Locate every Plasmodium parasite.
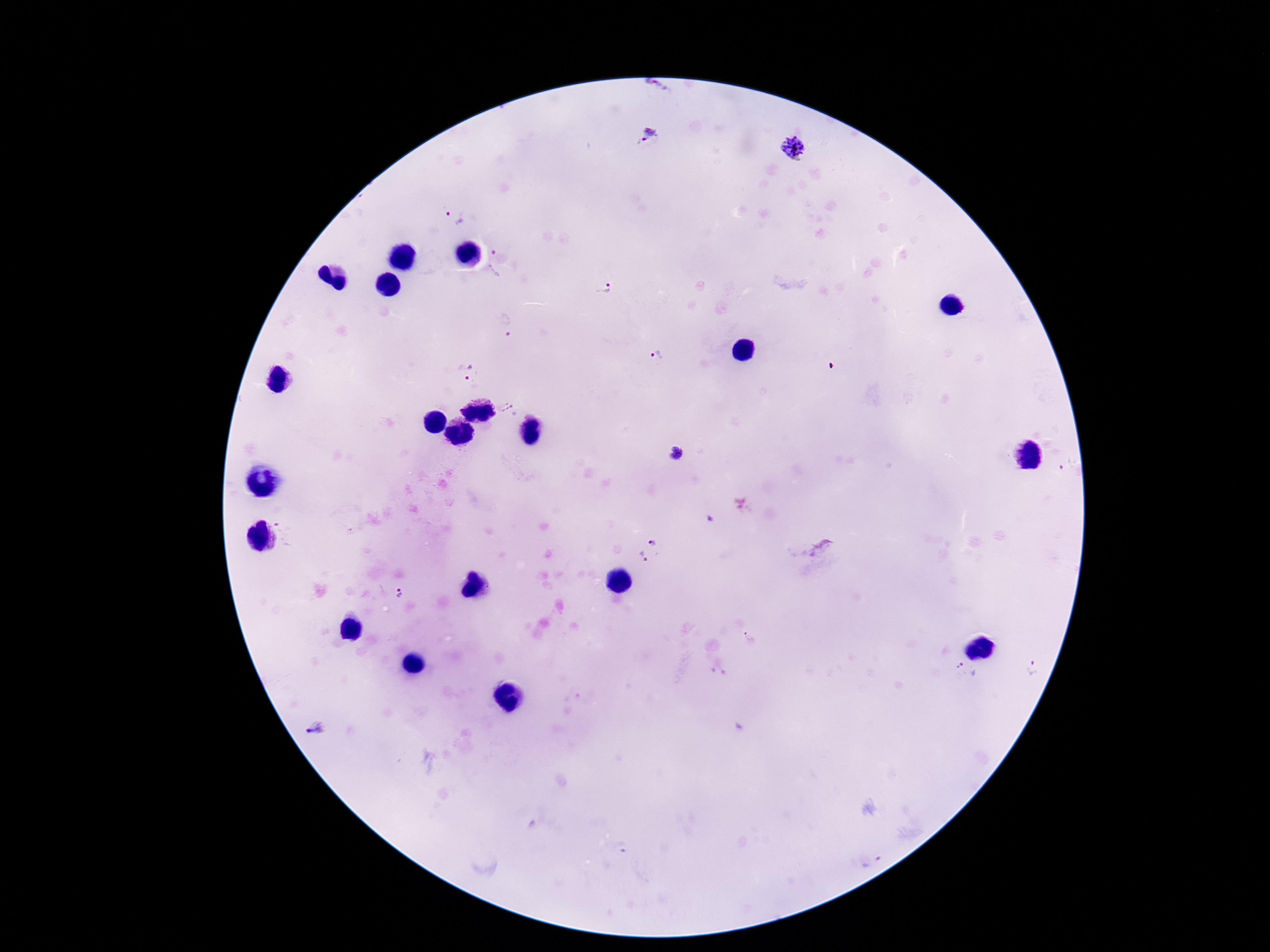
Approximate centers as (x, y) in pixels.
Plasmodium parasites: (658, 87), (649, 135), (794, 149), (454, 218), (502, 262), (605, 288), (506, 326), (657, 355), (470, 372), (508, 410), (675, 454), (1066, 464), (352, 532), (285, 534), (653, 541), (821, 548), (644, 558), (399, 593), (750, 639), (1029, 666), (963, 678), (316, 728), (621, 847), (872, 860).

field of view = one from this slide
magnification = 100x
preparation = thick blood film
stain = Giemsa
patient malaria status = infected
image size = 1270×952 pixels
capture = smartphone camera through the microscope eyepiece